Locate every leukocyte (white blood cell).
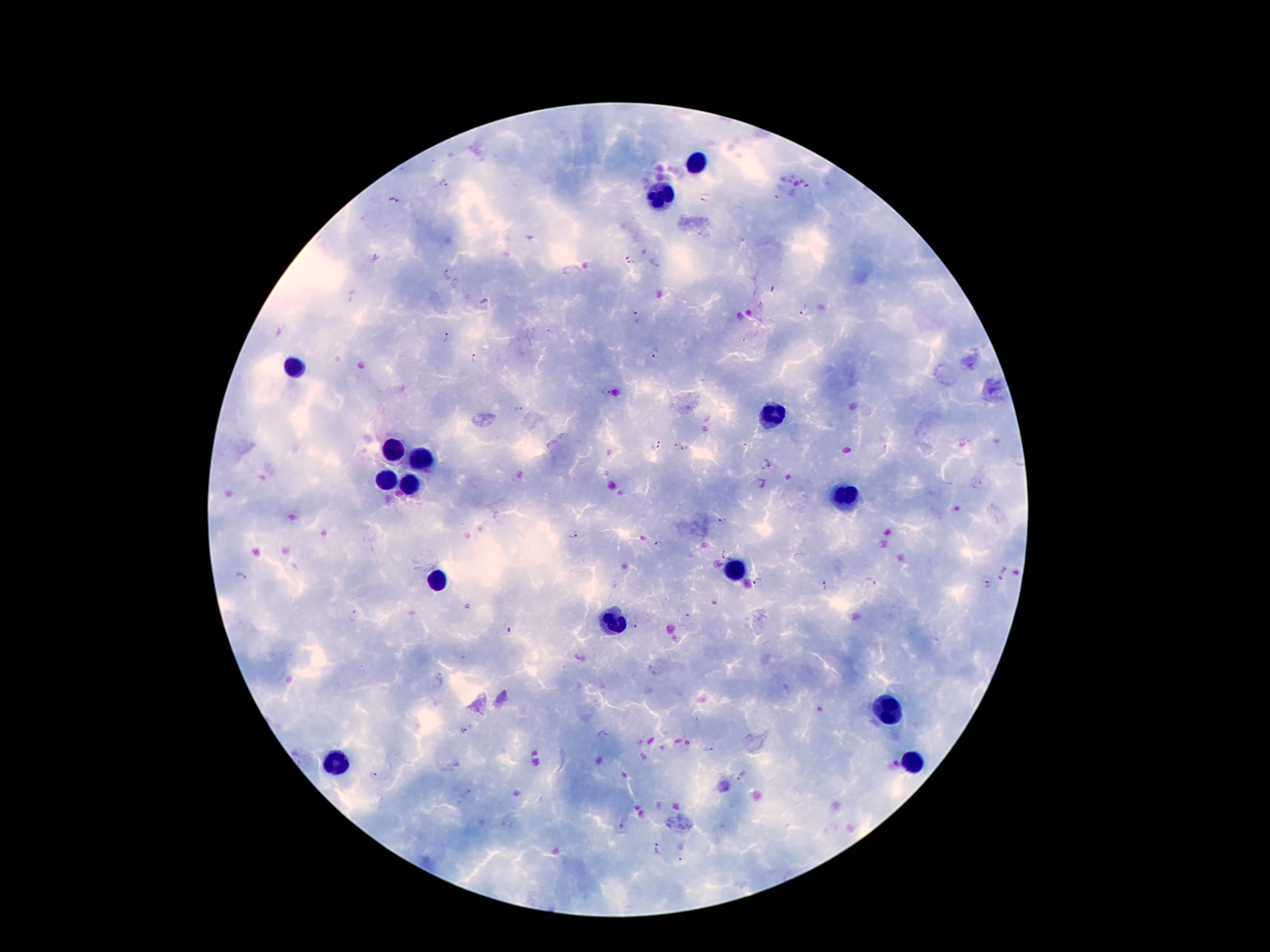
Approximate centers as [x, y] in pixels.
Leukocytes: [696, 162], [659, 196], [295, 368], [770, 418], [396, 451], [421, 460], [388, 481], [407, 486], [846, 496], [732, 567], [436, 580], [615, 626], [888, 709], [331, 763], [913, 764].

Plasmodium parasite locations: [443, 184], [807, 186], [706, 197], [394, 200], [375, 258], [630, 260], [448, 275], [484, 301], [804, 310], [636, 317], [446, 338], [655, 354], [474, 358], [605, 392], [517, 409], [745, 444], [657, 445], [677, 446], [686, 449], [766, 467], [762, 485], [722, 521], [574, 538], [658, 544], [241, 575], [869, 581], [758, 583], [988, 584], [825, 586], [355, 615], [508, 627], [635, 627], [464, 732], [604, 736], [709, 748], [374, 775], [741, 777], [656, 850], [681, 862]. Thick blood smear. Patient malaria status: positive for Plasmodium falciparum. One field from this slide. Giemsa stain. Image is 1270×952 pixels. Photographed through the microscope eyepiece with a smartphone camera. 100x magnification.